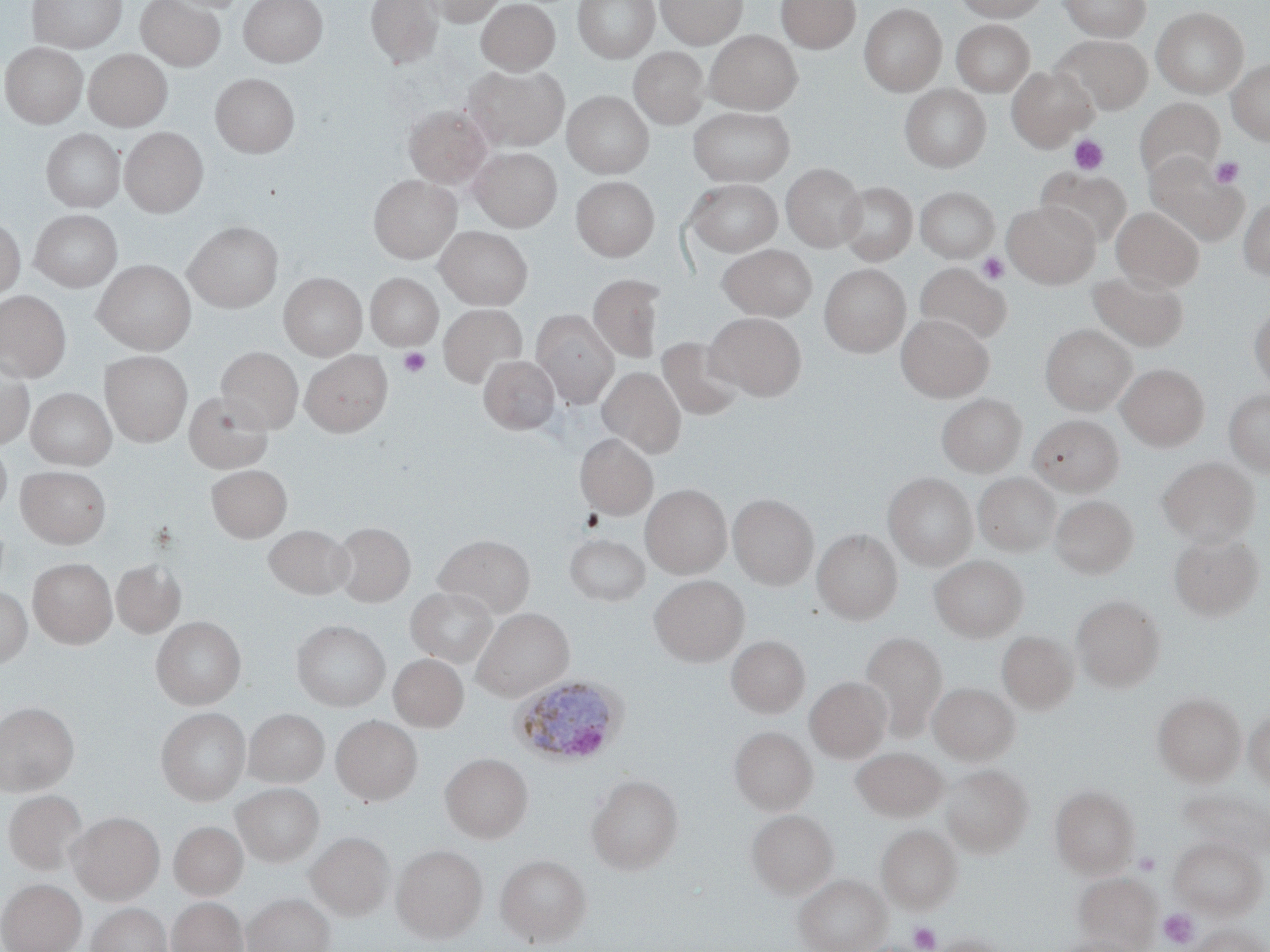
Summary:
  - Coordinate format: approximate bounding boxes as (x1,y1)-(x2,y2) corner pairs in pixels
  - Plasmodium ovale-infected red blood cell locations: (510,675)-(628,767)
  - Platelet locations: (1068,134)-(1109,175), (1209,156)-(1244,188), (977,252)-(1009,284), (398,348)-(430,376), (1135,851)-(1161,875), (1159,909)-(1199,948), (909,922)-(941,951)
  - Uninfected red blood cell locations: (27,0)-(127,52), (135,0)-(225,70), (238,0)-(328,67), (365,0)-(443,68), (420,0)-(507,27), (574,0)-(658,62), (656,0)-(747,47), (776,0)-(860,53), (953,0)-(1050,21), (1058,0)-(1151,40), (476,1)-(560,74), (859,4)-(946,95), (1151,6)-(1249,98), (951,19)-(1035,96), (705,30)-(801,114), (1054,35)-(1152,114), (1,42)-(87,128), (630,46)-(708,128), (83,49)-(172,131), (1228,59)-(1270,145), (465,65)-(569,150), (1006,66)-(1096,150), (211,72)-(299,156), (900,84)-(991,172), (562,91)-(654,178), (1134,98)-(1224,182), (404,105)-(491,187), (688,107)-(795,186), (120,127)-(207,216), (42,129)-(125,212), (471,147)-(561,231), (1144,153)-(1248,245), (781,164)-(865,251), (1038,169)-(1133,248), (369,175)-(460,262), (571,176)-(658,261), (685,179)-(783,256), (837,181)-(917,265), (915,186)-(1000,262), (1238,196)-(1270,282), (1003,201)-(1099,288), (1111,207)-(1204,290), (30,209)-(122,291), (0,218)-(25,301), (185,222)-(282,311), (435,226)-(533,309), (717,244)-(817,321), (93,260)-(196,354), (915,263)-(1010,346), (819,264)-(910,356), (1087,271)-(1188,352), (278,272)-(367,360), (366,272)-(444,350), (292,273)-(378,435), (587,274)-(665,362), (0,290)-(71,382), (438,304)-(526,387), (1248,304)-(1270,392), (531,310)-(619,407), (707,312)-(807,400), (896,313)-(993,401), (1040,323)-(1137,413), (657,337)-(745,420), (216,347)-(303,432), (300,350)-(393,436), (100,351)-(192,446), (0,354)-(35,449), (479,355)-(560,435), (1117,364)-(1209,450), (598,367)-(686,457), (26,387)-(117,470), (1224,389)-(1270,478), (183,390)-(273,473), (200,391)-(284,540), (937,394)-(1026,477), (1029,414)-(1124,496), (575,433)-(658,518), (0,442)-(12,520), (1157,457)-(1259,546), (206,464)-(291,542), (17,465)-(110,548), (883,473)-(977,570), (974,473)-(1059,556), (641,484)-(731,578), (728,494)-(818,589), (1051,495)-(1138,579), (333,522)-(415,606), (263,524)-(353,599), (813,529)-(902,624), (1168,532)-(1264,621), (433,533)-(535,616), (565,533)-(650,606), (930,555)-(1028,641), (28,558)-(117,648), (111,558)-(186,639), (649,575)-(749,665), (405,587)-(497,667), (0,589)-(32,667), (1072,595)-(1165,690), (472,608)-(574,701), (151,617)-(246,709), (292,619)-(390,711), (997,630)-(1079,714), (860,631)-(948,741), (726,636)-(809,718), (389,653)-(468,732), (805,677)-(891,762), (928,682)-(1019,764), (1152,692)-(1246,785), (0,701)-(78,795), (156,707)-(250,805), (1244,707)-(1270,790), (243,709)-(329,788), (331,715)-(422,805), (729,726)-(816,814), (851,747)-(948,821), (441,753)-(533,842), (942,764)-(1033,856), (586,774)-(683,873), (232,783)-(324,866), (1050,785)-(1139,877), (4,790)-(87,875), (747,809)-(837,897), (68,812)-(164,903), (170,821)-(247,899), (876,824)-(962,913), (307,831)-(394,920), (1168,835)-(1267,919), (392,844)-(487,942), (495,854)-(591,947), (794,873)-(890,952), (1074,873)-(1161,952), (0,879)-(86,952), (243,893)-(334,952), (167,897)-(247,952), (86,903)-(172,952), (1189,923)-(1268,952), (929,934)-(1008,952), (1053,935)-(1143,952)
  - Slide-level diagnosis: Plasmodium ovale
  - Stain: May-Grünwald-Giemsa
  - Image size: 1270×952 pixels
  - Magnification: 1000x
  - Modality: optical microscopy
  - Field of view: single
  - Preparation: thin blood smear